Assess this cell for malaria.
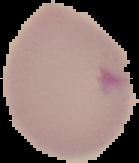

It is parasitized.

image size = 139×163 pixels
preparation = thin blood film
image type = segmented cell region on a black background